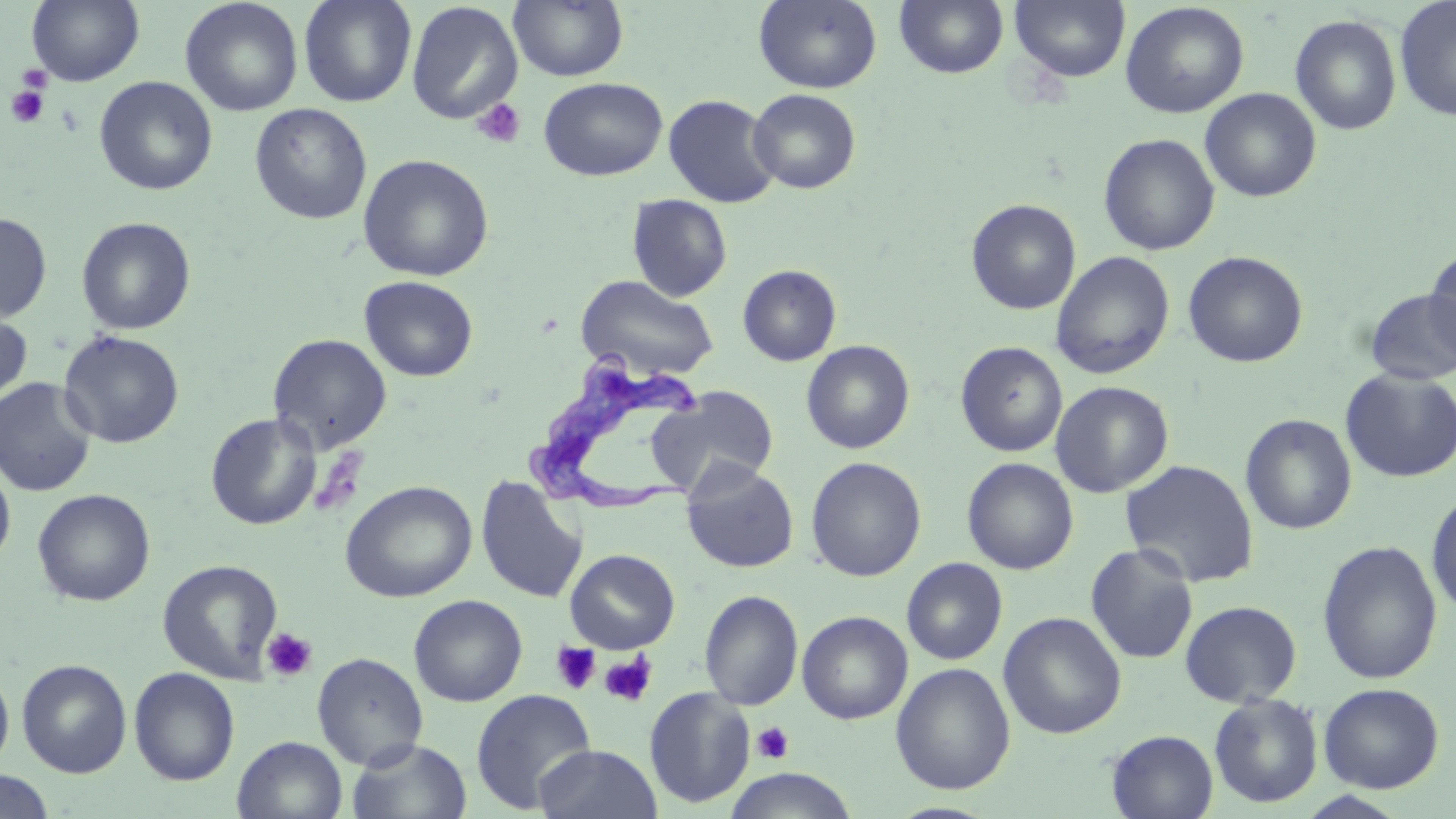
Summary:
  - Coordinate format: approximate bounding boxes as named x1/y1/x2/y2 corners in pixels
  - Trypanosoma brucei locations: (x1=525, y1=358, x2=710, y2=513)
  - Platelet locations: (x1=16, y1=64, x2=53, y2=92), (x1=6, y1=85, x2=49, y2=128), (x1=471, y1=98, x2=527, y2=150), (x1=262, y1=627, x2=317, y2=684), (x1=551, y1=642, x2=601, y2=695), (x1=599, y1=653, x2=658, y2=708), (x1=751, y1=722, x2=794, y2=764)
  - Uninfected red blood cell locations: (x1=26, y1=0, x2=145, y2=86), (x1=179, y1=0, x2=303, y2=117), (x1=299, y1=0, x2=417, y2=107), (x1=509, y1=0, x2=628, y2=82), (x1=753, y1=0, x2=882, y2=93), (x1=894, y1=0, x2=1009, y2=79), (x1=1010, y1=0, x2=1130, y2=83), (x1=1394, y1=0, x2=1456, y2=122), (x1=1120, y1=1, x2=1249, y2=118), (x1=406, y1=2, x2=523, y2=124), (x1=1290, y1=14, x2=1403, y2=135), (x1=94, y1=76, x2=217, y2=195), (x1=538, y1=77, x2=667, y2=181), (x1=748, y1=88, x2=861, y2=194), (x1=1200, y1=88, x2=1321, y2=202), (x1=663, y1=94, x2=781, y2=208), (x1=249, y1=103, x2=373, y2=225), (x1=1098, y1=133, x2=1220, y2=256), (x1=357, y1=154, x2=495, y2=282), (x1=627, y1=194, x2=732, y2=301), (x1=966, y1=198, x2=1081, y2=315), (x1=0, y1=212, x2=52, y2=323), (x1=76, y1=216, x2=196, y2=335), (x1=1423, y1=244, x2=1456, y2=366), (x1=1183, y1=250, x2=1308, y2=368), (x1=1050, y1=251, x2=1175, y2=379), (x1=737, y1=264, x2=841, y2=366), (x1=575, y1=274, x2=718, y2=379), (x1=359, y1=276, x2=478, y2=382), (x1=1364, y1=289, x2=1456, y2=385), (x1=0, y1=309, x2=33, y2=409), (x1=57, y1=330, x2=185, y2=449), (x1=268, y1=333, x2=391, y2=453), (x1=801, y1=340, x2=915, y2=454), (x1=955, y1=341, x2=1068, y2=457), (x1=1339, y1=368, x2=1456, y2=482), (x1=0, y1=377, x2=98, y2=497), (x1=1050, y1=380, x2=1174, y2=498), (x1=647, y1=386, x2=779, y2=496), (x1=204, y1=412, x2=322, y2=530), (x1=1240, y1=413, x2=1357, y2=535), (x1=806, y1=456, x2=926, y2=582), (x1=962, y1=457, x2=1079, y2=575), (x1=0, y1=459, x2=16, y2=572), (x1=1120, y1=459, x2=1260, y2=587), (x1=681, y1=461, x2=799, y2=574), (x1=476, y1=475, x2=587, y2=604), (x1=340, y1=480, x2=477, y2=603), (x1=32, y1=488, x2=155, y2=607), (x1=1426, y1=488, x2=1456, y2=618), (x1=1317, y1=540, x2=1442, y2=684), (x1=1085, y1=543, x2=1199, y2=665), (x1=564, y1=548, x2=680, y2=653), (x1=901, y1=557, x2=1008, y2=665), (x1=157, y1=559, x2=284, y2=684), (x1=699, y1=590, x2=804, y2=711), (x1=409, y1=594, x2=527, y2=707), (x1=1179, y1=599, x2=1303, y2=707), (x1=796, y1=611, x2=913, y2=724), (x1=998, y1=611, x2=1127, y2=739), (x1=312, y1=652, x2=428, y2=769), (x1=16, y1=658, x2=131, y2=778), (x1=890, y1=662, x2=1015, y2=795), (x1=129, y1=667, x2=240, y2=786), (x1=0, y1=669, x2=14, y2=771), (x1=1318, y1=683, x2=1445, y2=794), (x1=644, y1=687, x2=756, y2=808), (x1=470, y1=689, x2=596, y2=812), (x1=1208, y1=693, x2=1324, y2=809), (x1=1106, y1=730, x2=1219, y2=819), (x1=232, y1=736, x2=348, y2=819), (x1=346, y1=738, x2=472, y2=819), (x1=533, y1=744, x2=663, y2=819), (x1=723, y1=768, x2=859, y2=819), (x1=0, y1=770, x2=55, y2=818)
  - Slide-level diagnosis: Trypanosoma brucei
  - Modality: optical microscopy
  - Magnification: 1000x
  - Preparation: thin blood smear
  - Image size: 1456×819 pixels
  - Stain: May-Grünwald-Giemsa
  - Field of view: single